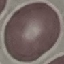
Summary:
  - Malaria status: uninfected
  - Preparation: thin blood smear
  - Image type: cell patch, automatically extracted from a larger field of view and resized to 64 × 64 pixels
  - Capture: smartphone through the microscope eyepiece
  - Stain: Giemsa